Outline each blood parasite and name the species.
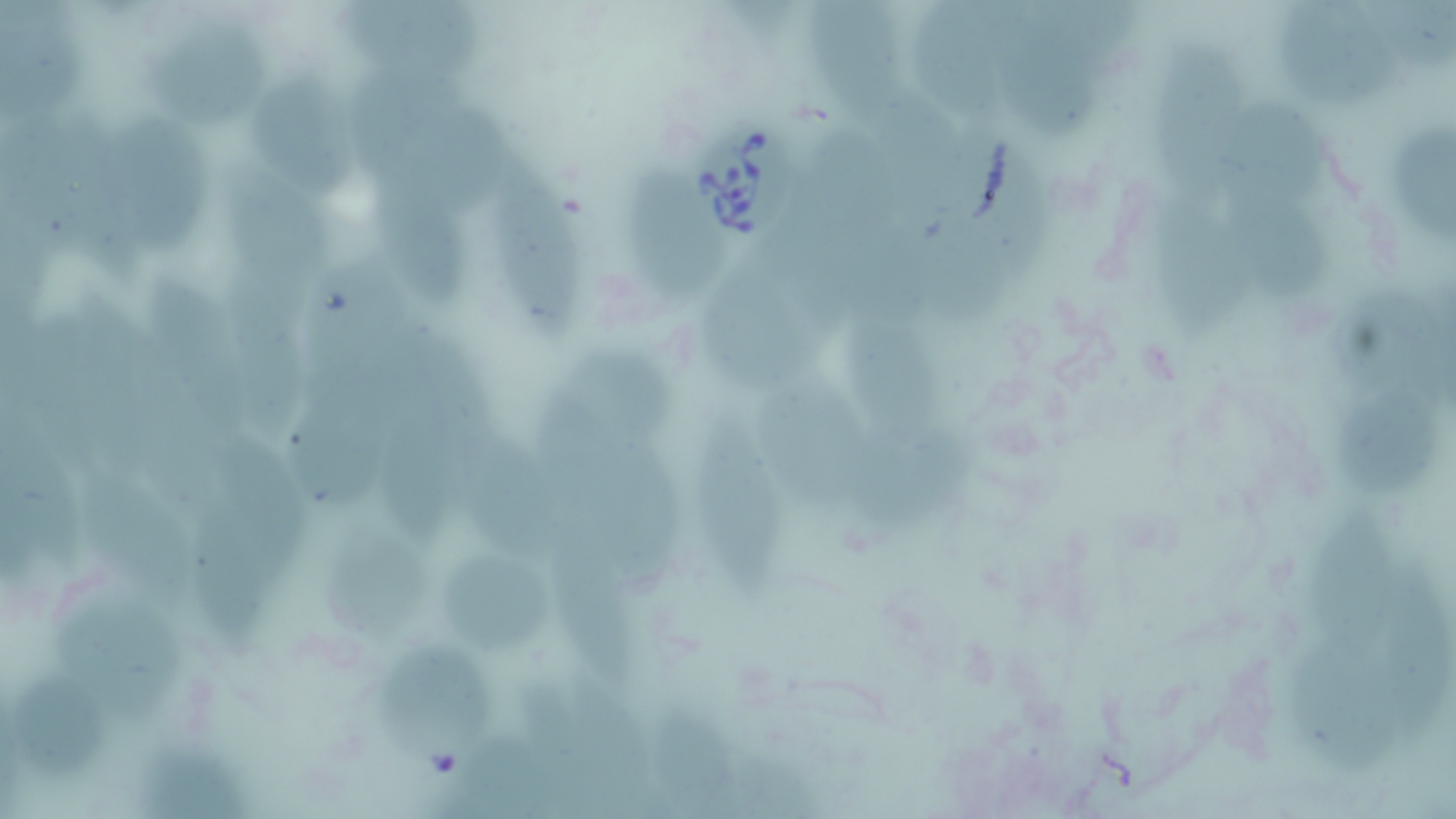

Approximate bounding boxes as named x1/y1/x2/y2 corners in pixels.
Babesia divergens-infected red blood cells: (x1=693, y1=118, x2=803, y2=240).
No Plasmodium falciparum, Plasmodium ovale, Plasmodium malariae, Plasmodium vivax, or Trypanosoma brucei observed.

slide-level diagnosis = Babesia divergens
magnification = 1000x
uninfected red blood cell locations = approximate bounding boxes as named x1/y1/x2/y2 corners in pixels: (x1=333, y1=0, x2=498, y2=78), (x1=806, y1=0, x2=904, y2=126), (x1=1003, y1=0, x2=1109, y2=156), (x1=1042, y1=0, x2=1154, y2=59), (x1=909, y1=2, x2=1021, y2=141), (x1=147, y1=22, x2=278, y2=131), (x1=1160, y1=39, x2=1248, y2=207), (x1=340, y1=66, x2=467, y2=179), (x1=251, y1=75, x2=354, y2=197), (x1=1224, y1=91, x2=1313, y2=209), (x1=406, y1=93, x2=518, y2=205), (x1=104, y1=107, x2=218, y2=269), (x1=895, y1=110, x2=998, y2=221), (x1=811, y1=132, x2=888, y2=218), (x1=981, y1=140, x2=1073, y2=284), (x1=221, y1=154, x2=330, y2=280), (x1=487, y1=160, x2=597, y2=345), (x1=378, y1=169, x2=473, y2=307), (x1=636, y1=171, x2=728, y2=305), (x1=1241, y1=188, x2=1312, y2=303), (x1=1153, y1=195, x2=1258, y2=354), (x1=789, y1=198, x2=870, y2=345), (x1=860, y1=224, x2=951, y2=356), (x1=938, y1=239, x2=1027, y2=336), (x1=240, y1=257, x2=320, y2=364), (x1=697, y1=261, x2=816, y2=379), (x1=312, y1=266, x2=428, y2=378), (x1=149, y1=275, x2=242, y2=434), (x1=217, y1=284, x2=325, y2=442), (x1=863, y1=318, x2=957, y2=442), (x1=412, y1=331, x2=502, y2=441), (x1=576, y1=336, x2=679, y2=447), (x1=737, y1=363, x2=858, y2=503), (x1=525, y1=373, x2=614, y2=528), (x1=301, y1=398, x2=391, y2=508), (x1=385, y1=404, x2=465, y2=557), (x1=855, y1=404, x2=1006, y2=527), (x1=696, y1=407, x2=778, y2=598), (x1=465, y1=421, x2=556, y2=569), (x1=217, y1=429, x2=322, y2=579), (x1=618, y1=455, x2=690, y2=596), (x1=104, y1=469, x2=200, y2=612), (x1=194, y1=496, x2=284, y2=657), (x1=563, y1=528, x2=647, y2=672), (x1=320, y1=534, x2=437, y2=638), (x1=450, y1=550, x2=565, y2=656), (x1=104, y1=586, x2=198, y2=687), (x1=389, y1=639, x2=487, y2=689)
modality = optical microscopy
field of view = one of a larger specimen
preparation = thin blood smear
image size = 1456×819 pixels
stain = May-Grünwald-Giemsa